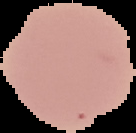 Result: no malaria parasites seen. From a thin blood film. Image is 136×133 pixels. Cell region segmented out of the field of view; the surrounding area is masked to black.